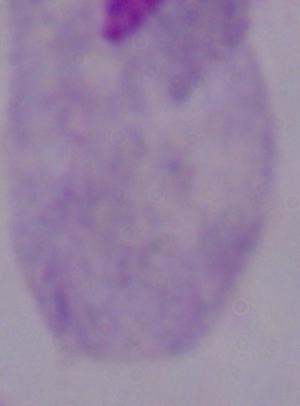
{
  "magnification": "1000x",
  "identification": "trichomonad",
  "modality": "photomicrograph"
}